Classify this cell by malaria status.
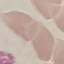

It is uninfected.

{
  "preparation": "thin blood film",
  "stain": "Giemsa",
  "capture": "smartphone through the microscope eyepiece",
  "image_type": "automatically extracted cell patch, resized to 64 × 64 pixels"
}